Report the malaria status of this cell.
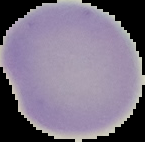

Uninfected.

Summary:
  - Image type: segmented cell region on a black background
  - Image size: 145×142 pixels
  - Preparation: thin blood smear